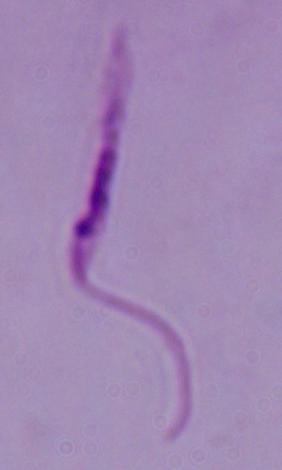

Summary:
  - Modality: photomicrograph
  - Identification: Leishmania
  - Magnification: 1000x